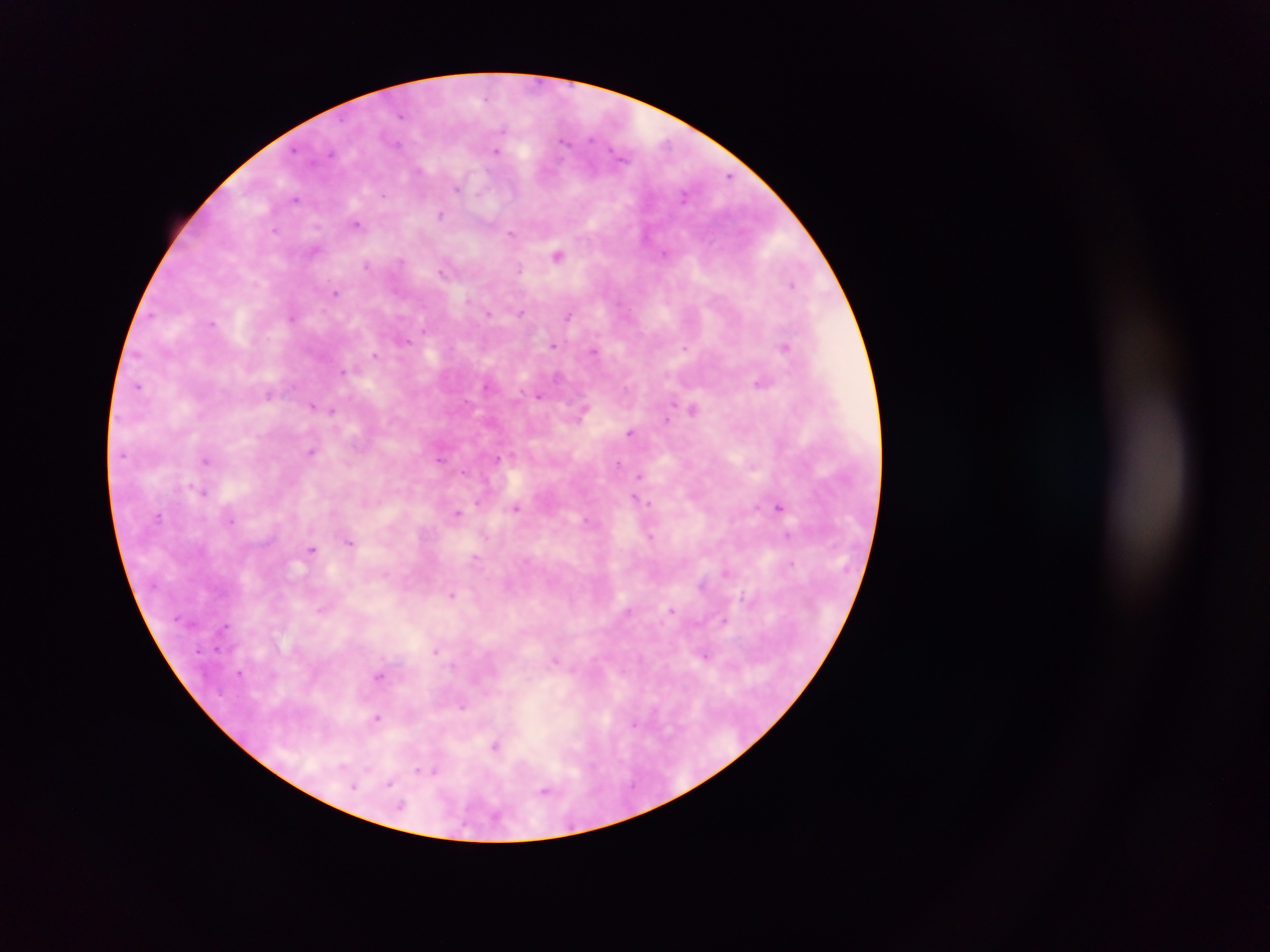

preparation = thick blood film
country = Ghana
Plasmodium parasite locations = approximate centers as {x, y} in pixels: {402, 115}, {504, 130}, {591, 138}, {564, 141}, {398, 142}, {496, 151}, {621, 156}, {419, 170}, {728, 176}, {458, 189}, {383, 195}, {684, 196}, {295, 198}, {441, 214}, {357, 223}, {317, 226}, {274, 230}, {511, 233}, {314, 251}, {664, 253}, {558, 256}, {401, 260}, {366, 265}, {518, 270}, {442, 271}, {793, 285}, {335, 292}, {468, 299}, {521, 313}, {489, 314}, {570, 315}, {292, 317}, {213, 323}, {424, 330}, {406, 341}, {553, 346}, {786, 347}, {685, 348}, {595, 351}, {375, 355}, {342, 371}, {761, 383}, {139, 386}, {486, 386}, {268, 395}, {539, 396}, {312, 406}, {692, 409}, {332, 410}, {581, 413}, {666, 420}, {630, 432}, {311, 450}, {498, 458}, {439, 460}, {205, 461}, {619, 463}, {464, 472}, {639, 476}, {203, 491}, {636, 498}, {648, 502}, {779, 507}, {515, 508}, {458, 512}, {158, 515}, {231, 521}, {588, 521}, {788, 534}, {651, 536}, {351, 542}, {311, 550}, {475, 557}, {793, 563}, {452, 594}, {322, 609}, {628, 610}, {672, 611}, {724, 621}, {435, 651}, {705, 656}, {555, 660}, {239, 672}, {378, 676}, {462, 706}, {377, 718}, {634, 723}, {495, 746}, {342, 767}, {367, 769}, {427, 771}, {389, 783}, {354, 787}, {544, 791}, {400, 807}
capture = mobile-phone photograph through a microscope
field of view = single
image size = 1270×952 pixels